Assess this cell for malaria.
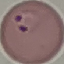

Parasitized.

image_type: automatically extracted cell patch, resized to 64 × 64 pixels
capture: smartphone camera at the microscope eyepiece
stain: Giemsa
preparation: thin smear